Comment on the morphology of the red blood cells.
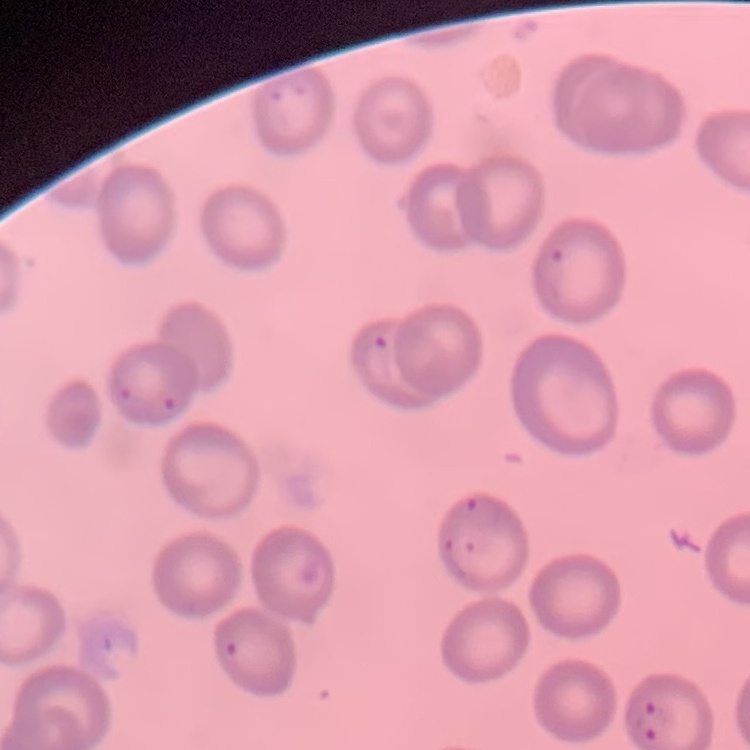

No rouleaux formation.

Thin blood film. One tile cut from a larger photomicrograph. Field's or Giemsa stain.